Report the malaria status of this cell.
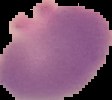

Parasitized.

Cell region segmented out of the field of view; the surrounding area is masked to black. Image is 112×100 pixels. From a thin blood smear.